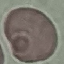
Summary:
  - Malaria status: uninfected
  - Stain: Giemsa
  - Image type: cell patch, automatically extracted from a larger field of view and resized to 64 × 64 pixels
  - Preparation: thin blood film
  - Capture: smartphone through the microscope eyepiece